Outline each blood parasite and name the species.
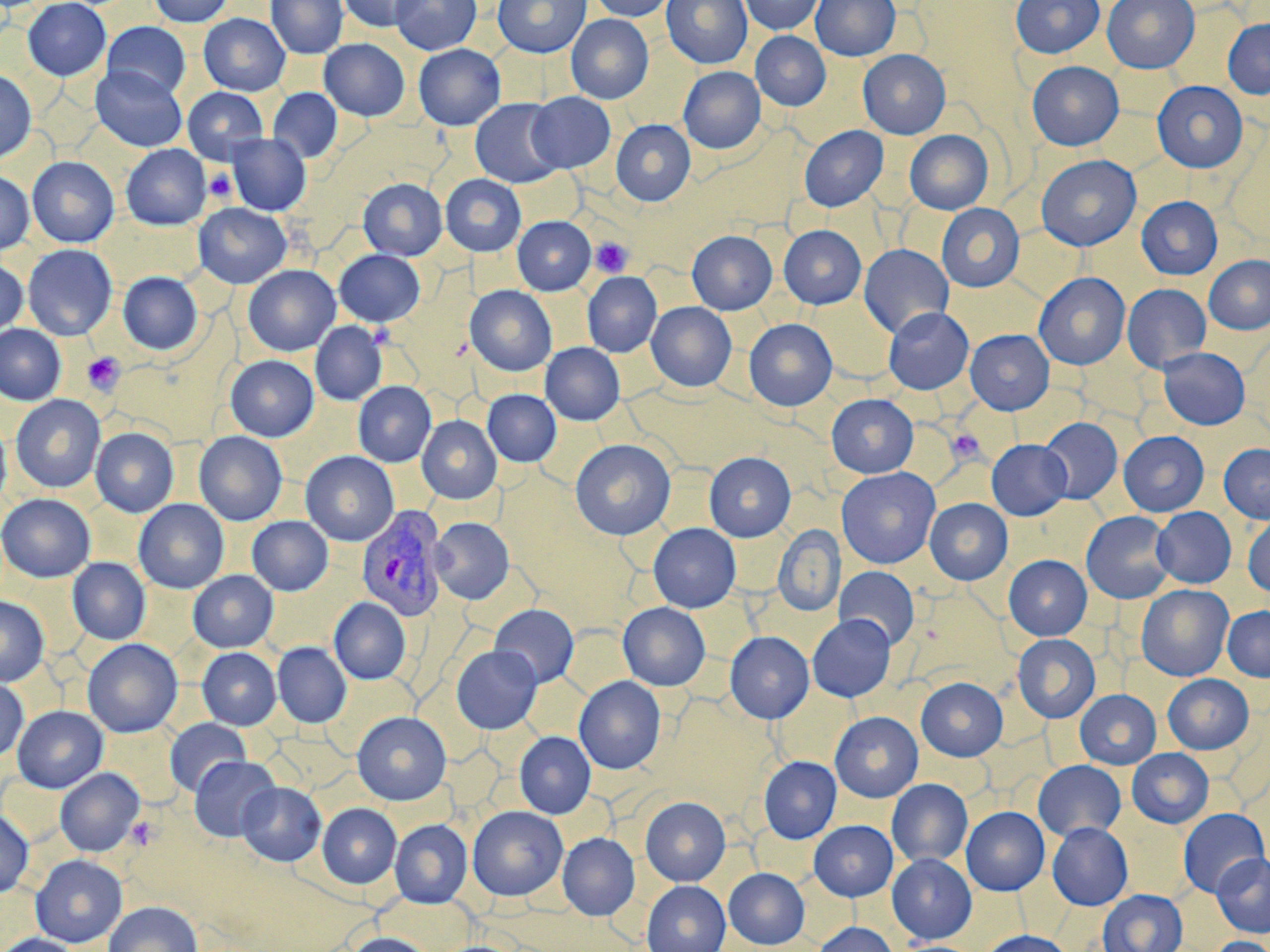
Approximate bounding boxes as [x1, y1, x2, y2] in pixels.
Plasmodium vivax-infected red blood cells: [357, 505, 449, 623].
No Plasmodium falciparum, Plasmodium ovale, Plasmodium malariae, Babesia divergens, or Trypanosoma brucei observed.

Summary:
  - Platelet locations: [205, 169, 237, 202], [590, 237, 633, 277], [368, 323, 396, 349], [82, 352, 126, 395], [946, 428, 986, 464], [126, 816, 160, 850]
  - Uninfected red blood cell locations: [23, 0, 111, 81], [148, 0, 235, 27], [266, 0, 347, 59], [339, 0, 424, 32], [390, 0, 481, 55], [493, 0, 590, 58], [589, 0, 676, 21], [662, 0, 752, 68], [740, 0, 823, 35], [811, 0, 900, 60], [1011, 0, 1104, 58], [1102, 0, 1199, 73], [199, 13, 290, 95], [566, 14, 653, 104], [1222, 18, 1270, 98], [103, 22, 190, 99], [751, 31, 831, 110], [319, 38, 410, 121], [413, 44, 505, 130], [858, 49, 950, 139], [1027, 61, 1123, 150], [90, 65, 187, 152], [679, 66, 765, 154], [0, 69, 36, 164], [1152, 80, 1248, 172], [183, 87, 268, 163], [268, 88, 342, 162], [526, 92, 615, 173], [470, 98, 565, 188], [612, 119, 695, 206], [799, 125, 888, 212], [904, 130, 993, 215], [226, 134, 311, 215], [121, 144, 210, 230], [1036, 154, 1141, 251], [27, 156, 119, 247], [0, 170, 34, 255], [440, 174, 526, 256], [358, 178, 447, 260], [1136, 196, 1222, 279], [193, 203, 292, 288], [936, 204, 1024, 292], [512, 216, 595, 295], [779, 225, 866, 309], [687, 230, 778, 314], [22, 244, 117, 341], [858, 244, 954, 338], [334, 250, 425, 326], [1204, 255, 1270, 335], [0, 257, 28, 335], [243, 265, 341, 356], [118, 272, 202, 354], [582, 272, 662, 357], [1033, 272, 1131, 370], [1122, 283, 1211, 372], [465, 285, 557, 376], [646, 302, 736, 392], [883, 307, 974, 394], [744, 319, 837, 410], [311, 321, 387, 405], [0, 324, 66, 405], [965, 329, 1054, 414], [540, 343, 625, 425], [1158, 347, 1250, 429], [225, 355, 319, 441], [353, 381, 436, 467], [482, 389, 561, 467], [11, 394, 106, 493], [826, 394, 918, 477], [417, 415, 501, 504], [1039, 417, 1123, 504], [0, 418, 12, 509], [91, 427, 178, 517], [194, 431, 287, 525], [1119, 431, 1209, 516], [570, 439, 676, 540], [987, 440, 1071, 520], [1219, 443, 1270, 523], [300, 451, 399, 546], [704, 452, 796, 541], [836, 467, 940, 568], [0, 493, 95, 582], [925, 498, 1012, 585], [133, 499, 229, 593], [1152, 507, 1236, 588], [1081, 511, 1175, 603], [1242, 514, 1270, 597], [247, 516, 333, 595], [430, 517, 514, 604], [648, 523, 741, 613], [772, 525, 844, 615], [1004, 555, 1092, 640], [67, 558, 150, 644], [834, 567, 920, 650], [188, 570, 278, 652], [1136, 584, 1233, 681], [0, 596, 49, 686], [329, 597, 411, 684], [618, 602, 710, 690], [489, 604, 579, 688], [1222, 605, 1270, 681], [807, 614, 895, 702], [725, 632, 813, 722], [1012, 634, 1100, 723], [82, 639, 182, 737], [273, 642, 351, 727], [451, 645, 542, 734], [198, 647, 281, 729], [1163, 674, 1253, 753], [574, 676, 666, 774], [916, 677, 1007, 761], [0, 678, 28, 762], [1074, 690, 1161, 769], [12, 705, 108, 793], [352, 711, 451, 804], [830, 711, 923, 802], [165, 718, 251, 797], [515, 731, 596, 818], [1127, 748, 1214, 828], [189, 755, 280, 841], [758, 756, 841, 843], [1033, 760, 1126, 841], [55, 768, 145, 856], [886, 779, 972, 867], [237, 781, 326, 866], [641, 797, 730, 886], [317, 803, 401, 888], [468, 806, 567, 900], [961, 806, 1049, 895], [0, 808, 34, 898], [1178, 808, 1269, 897], [390, 819, 472, 908], [809, 820, 898, 900], [1047, 822, 1133, 910], [557, 832, 639, 919], [1212, 852, 1270, 937], [30, 854, 127, 947], [887, 854, 976, 942], [724, 868, 810, 948], [642, 880, 731, 952], [1097, 889, 1188, 952], [103, 901, 203, 952], [812, 922, 899, 952], [979, 930, 1075, 952], [343, 932, 434, 952], [0, 933, 81, 952], [1208, 936, 1270, 952]
  - Slide-level diagnosis: Plasmodium vivax
  - Image size: 1270×952 pixels
  - Field of view: single
  - Modality: light microscopy
  - Magnification: 1000x
  - Stain: May-Grünwald-Giemsa
  - Preparation: thin blood film